Assess this cell for malaria.
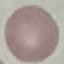
Uninfected.

Summary:
  - Image type: cell patch, automatically extracted from a larger field of view and resized to 64 × 64 pixels
  - Preparation: thin blood smear
  - Stain: Giemsa
  - Capture: smartphone through the microscope eyepiece